Locate every leukocyte (white blood cell).
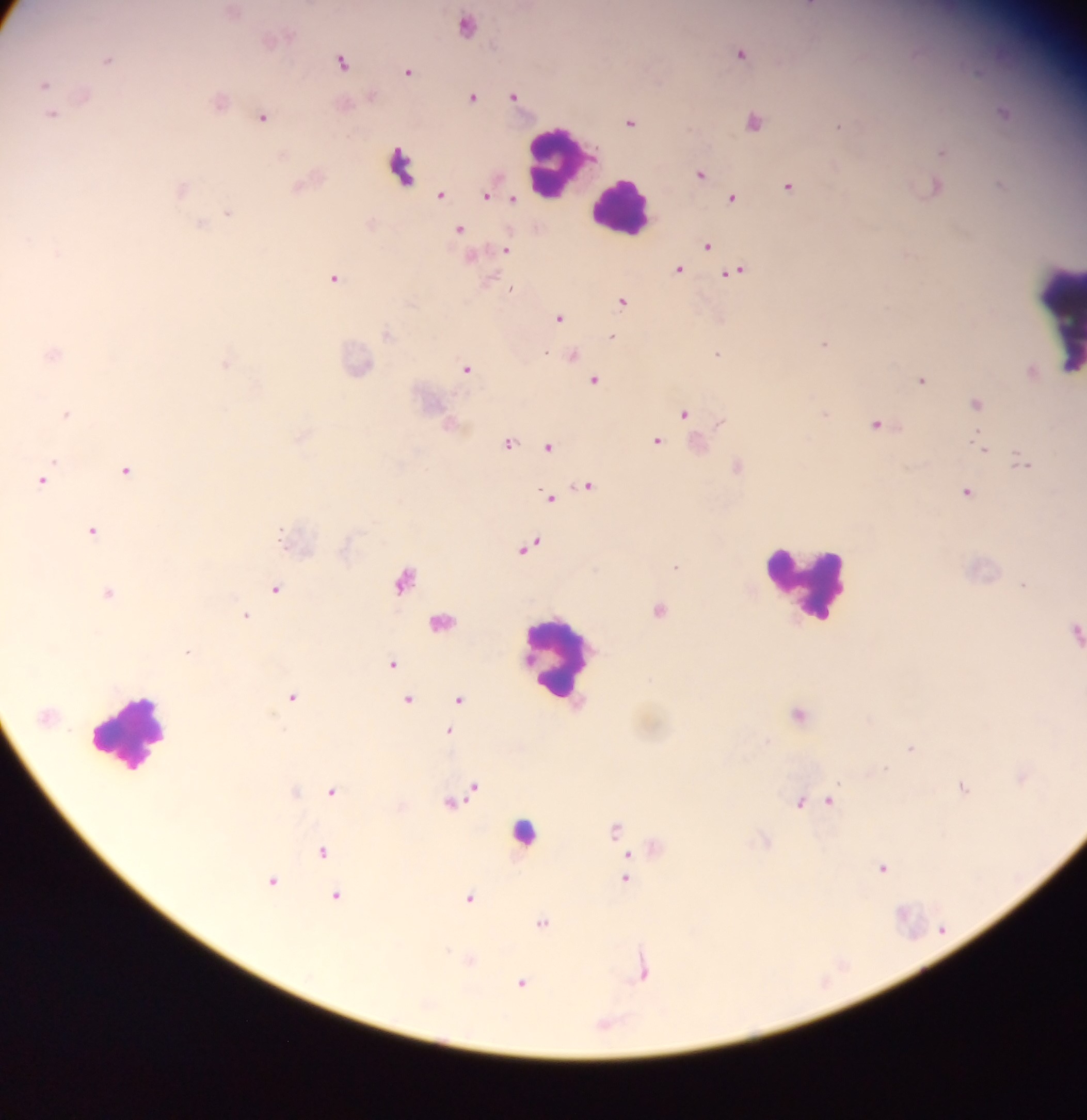

Approximate centers as (x, y) in pixels.
Leukocytes: (557, 163), (401, 167), (622, 204), (1059, 318), (809, 589), (559, 659), (131, 733), (523, 828).

country = Ghana
capture = mobile-phone photograph through a microscope
malaria parasite locations = approximate centers as (x, y) in pixels: (808, 5), (466, 25), (740, 52), (107, 59), (342, 62), (408, 71), (44, 84), (513, 95), (473, 96), (51, 115), (262, 117), (753, 121), (630, 122), (838, 126), (941, 151), (701, 173), (999, 185), (934, 186), (788, 187), (439, 194), (485, 196), (732, 198), (510, 200), (228, 213), (201, 224), (459, 229), (706, 245), (506, 249), (678, 269), (734, 271), (334, 278), (622, 301), (558, 317), (611, 337), (823, 344), (717, 354), (571, 356), (225, 364), (467, 368), (594, 380), (921, 380), (976, 403), (683, 413), (66, 414), (824, 414), (877, 424), (656, 441), (508, 444), (548, 446), (982, 448), (1021, 461), (737, 466), (125, 470), (43, 480), (586, 485), (966, 491), (548, 497), (92, 531), (530, 547), (675, 566), (405, 579), (1022, 584), (275, 589), (108, 592), (658, 609), (246, 615), (441, 621), (187, 651), (392, 663), (292, 697), (408, 699), (459, 700), (798, 713), (448, 731), (766, 740), (911, 748), (885, 769), (1021, 777), (962, 786), (471, 787), (331, 791), (462, 796), (829, 801), (799, 802), (614, 828), (321, 850), (627, 857), (882, 867), (625, 878), (274, 880), (335, 895), (469, 898), (541, 922), (642, 972), (521, 983)
field of view = single
preparation = thick blood film
image size = 1087×1120 pixels